Comment on the morphology of the erythrocytes.
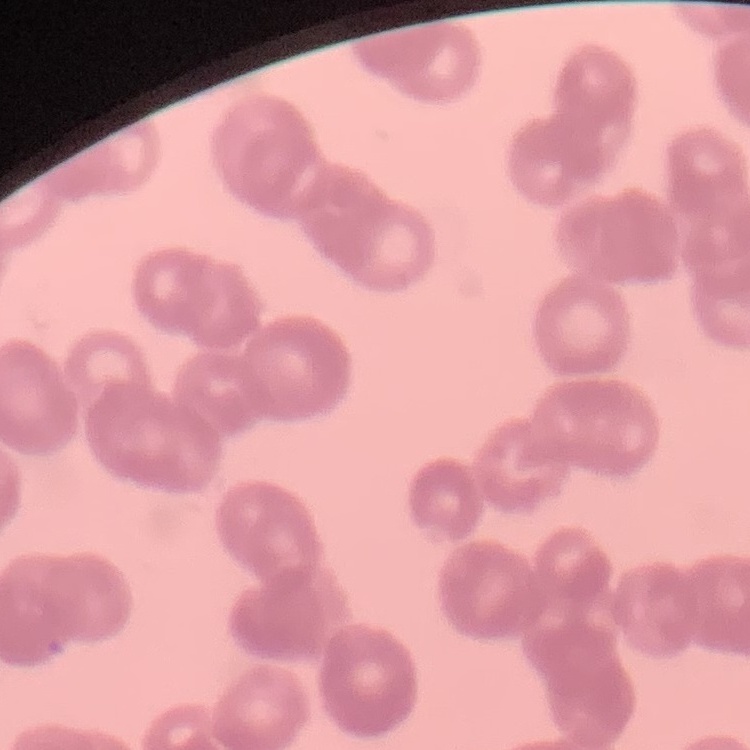

Rouleaux formation.

stain = Field's or Giemsa
preparation = thin blood film
image type = one tile cut from a larger photomicrograph